Locate and identify every blood parasite.
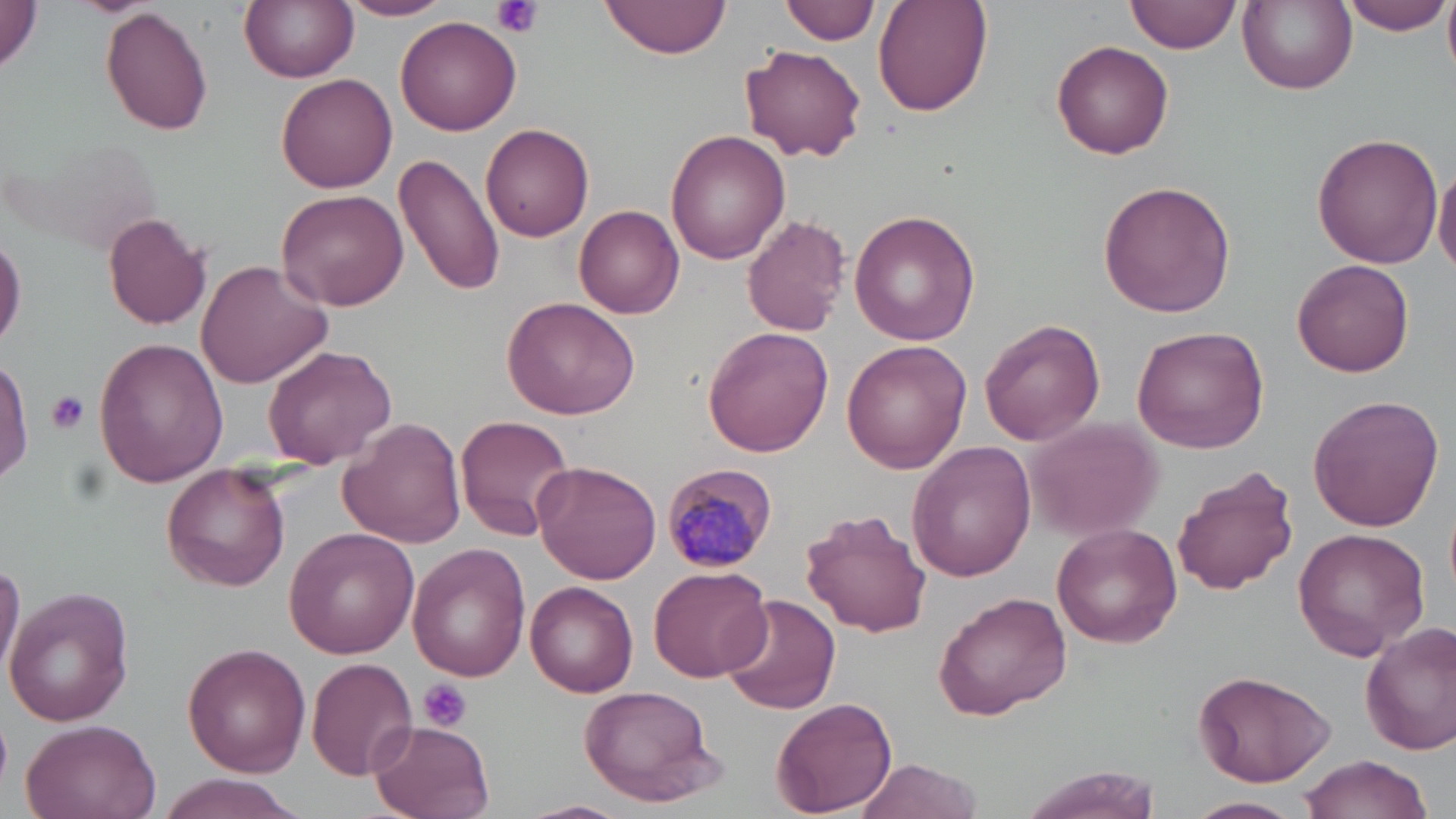
Approximate bounding boxes as (x1,y1)-(x2,y2) corner pairs in pixels.
Plasmodium malariae-infected red blood cells: (659,460)-(776,574).
No Plasmodium falciparum, Plasmodium ovale, Plasmodium vivax, Babesia divergens, or Trypanosoma brucei observed.

slide-level diagnosis = Plasmodium malariae
stain = May-Grünwald-Giemsa
image size = 1456×819 pixels
field of view = one of a larger specimen
uninfected red blood cell locations = approximate bounding boxes as (x1,y1)-(x2,y2) corner pairs in pixels: (239,0)-(358,84), (337,0)-(454,21), (601,0)-(732,58), (784,0)-(878,44), (874,0)-(995,118), (1128,0)-(1237,55), (1237,0)-(1357,94), (1340,0)-(1452,35), (1443,0)-(1456,75), (1,1)-(46,73), (99,6)-(215,136), (396,16)-(523,136), (1052,40)-(1175,160), (741,44)-(867,163), (277,71)-(397,193), (480,123)-(595,241), (666,129)-(791,265), (1312,133)-(1442,268), (12,140)-(159,253), (394,152)-(506,297), (1434,165)-(1456,277), (1097,181)-(1237,319), (276,188)-(408,313), (574,203)-(684,318), (849,209)-(981,345), (101,212)-(213,331), (742,213)-(850,336), (0,230)-(25,351), (1292,256)-(1413,377), (196,257)-(333,390), (501,298)-(641,421), (981,320)-(1104,444), (1131,325)-(1269,453), (703,326)-(834,456), (93,336)-(228,488), (840,340)-(971,475), (262,346)-(397,467), (0,350)-(34,488), (1307,393)-(1445,531), (455,414)-(576,540), (1024,415)-(1166,540), (337,418)-(466,549), (908,442)-(1040,582), (532,460)-(661,584), (159,465)-(289,591), (1172,466)-(1298,595), (800,509)-(932,638), (1052,523)-(1183,648), (283,527)-(422,657), (1291,527)-(1429,662), (406,543)-(532,681), (0,554)-(24,686), (648,565)-(772,681), (526,581)-(639,698), (2,585)-(135,726), (933,591)-(1071,718), (717,594)-(838,718), (1361,622)-(1456,756), (183,644)-(310,774), (307,657)-(418,779), (1192,669)-(1334,786), (577,683)-(724,809), (770,696)-(898,815), (20,716)-(164,819), (367,718)-(496,819), (1297,754)-(1434,818), (855,756)-(986,819), (1011,765)-(1159,819), (150,774)-(306,819), (1186,796)-(1301,819), (513,800)-(631,819)
magnification = 1000x
platelet locations = approximate bounding boxes as (x1,y1)-(x2,y2) corner pairs in pixels: (491,0)-(542,39), (46,390)-(92,435), (419,679)-(471,731)
modality = light microscopy
preparation = thin blood smear